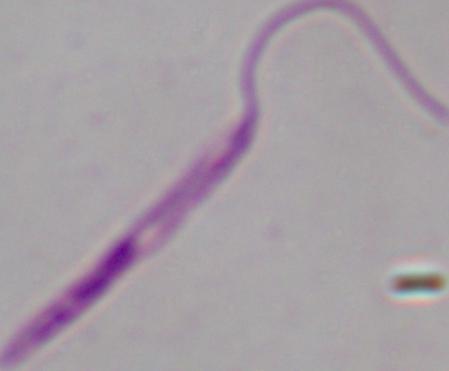 Photomicrograph. Captured at 1000x magnification. A Leishmania parasite is shown.